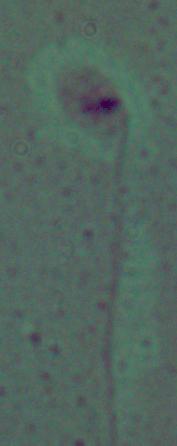

modality: photomicrograph
identification: Leishmania
magnification: 1000x